Locate and identify every blood parasite.
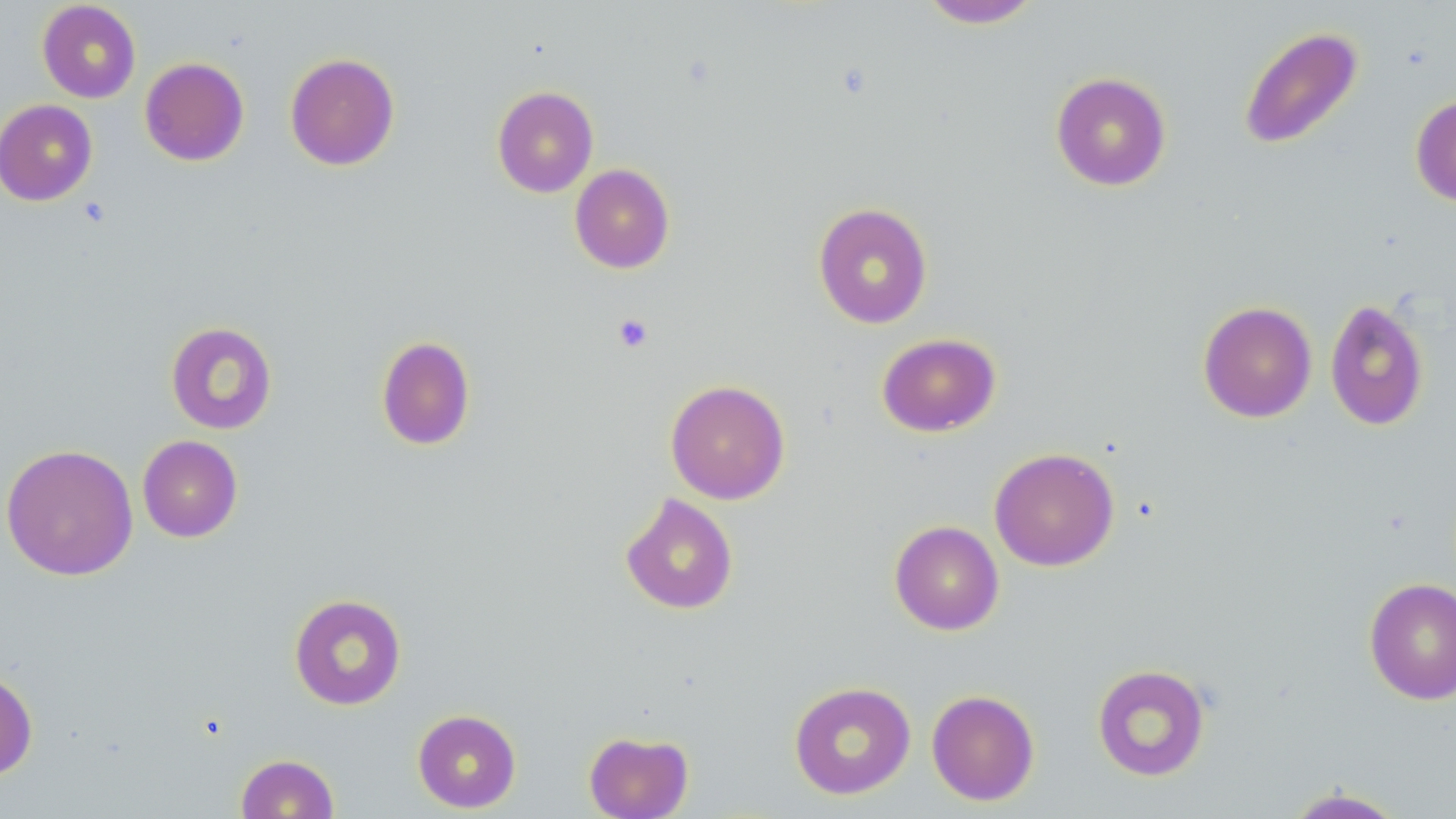
No blood parasites observed.

slide-level diagnosis = negative for blood parasites
magnification = 1000x
stain = May-Grünwald-Giemsa
preparation = thin blood film
image size = 1456×819 pixels
field of view = single
modality = light microscopy
platelet locations = approximate bounding boxes as named x1/y1/x2/y2 corners in pixels: (x1=612, y1=313, x2=654, y2=352)
uninfected red blood cell locations = approximate bounding boxes as named x1/y1/x2/y2 corners in pixels: (x1=918, y1=0, x2=1044, y2=29), (x1=37, y1=1, x2=141, y2=103), (x1=1238, y1=25, x2=1364, y2=150), (x1=284, y1=53, x2=400, y2=170), (x1=140, y1=57, x2=249, y2=166), (x1=1050, y1=72, x2=1172, y2=191), (x1=492, y1=86, x2=599, y2=197), (x1=1410, y1=93, x2=1456, y2=207), (x1=0, y1=99, x2=99, y2=206), (x1=570, y1=164, x2=675, y2=273), (x1=813, y1=202, x2=933, y2=329), (x1=1324, y1=298, x2=1429, y2=431), (x1=1198, y1=301, x2=1317, y2=423), (x1=165, y1=321, x2=277, y2=434), (x1=876, y1=332, x2=1001, y2=437), (x1=376, y1=336, x2=476, y2=451), (x1=665, y1=379, x2=790, y2=505), (x1=137, y1=435, x2=243, y2=542), (x1=0, y1=443, x2=138, y2=581), (x1=989, y1=447, x2=1119, y2=571), (x1=620, y1=492, x2=739, y2=615), (x1=889, y1=520, x2=1004, y2=635), (x1=1363, y1=576, x2=1456, y2=704), (x1=289, y1=593, x2=406, y2=710), (x1=1092, y1=663, x2=1211, y2=782), (x1=0, y1=668, x2=38, y2=780), (x1=788, y1=681, x2=916, y2=800), (x1=926, y1=689, x2=1040, y2=806), (x1=412, y1=709, x2=521, y2=813), (x1=584, y1=730, x2=694, y2=819), (x1=235, y1=753, x2=339, y2=818), (x1=1281, y1=786, x2=1411, y2=818)